Identify the cell.
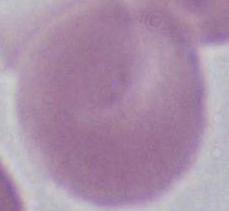

This is an erythrocyte.

Captured at 1000x magnification. Photomicrograph.